Classify this cell by malaria status.
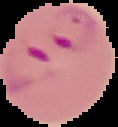
Parasitized.

image size = 118×127 pixels
image type = segmented cell region with the area outside set to black
preparation = thin blood smear